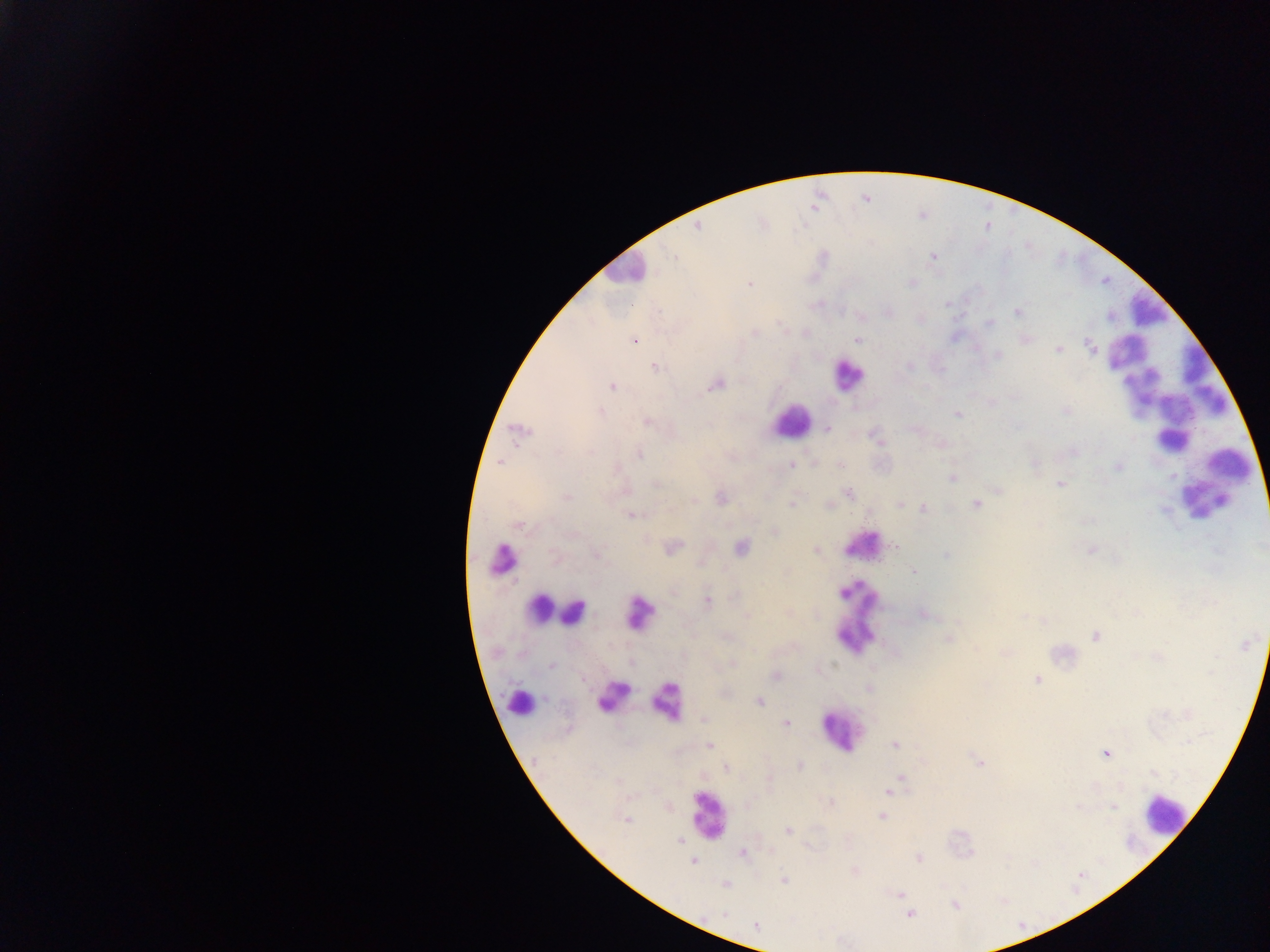

capture = mobile-phone photograph through a microscope
malaria parasite locations = approximate centers as {x, y} in pixels: {866, 199}, {697, 227}, {674, 257}, {932, 258}, {749, 283}, {910, 283}, {946, 304}, {887, 312}, {1017, 313}, {861, 316}, {988, 322}, {634, 340}, {858, 340}, {1025, 340}, {1091, 348}, {1058, 349}, {998, 355}, {909, 365}, {655, 367}, {715, 385}, {612, 386}, {991, 402}, {598, 409}, {1067, 410}, {956, 414}, {647, 422}, {826, 428}, {915, 428}, {518, 431}, {876, 438}, {941, 444}, {1074, 451}, {639, 454}, {500, 461}, {813, 464}, {839, 465}, {1035, 465}, {1118, 465}, {790, 466}, {953, 478}, {656, 484}, {1060, 484}, {997, 489}, {848, 493}, {565, 497}, {721, 498}, {691, 502}, {791, 503}, {827, 504}, {899, 504}, {976, 504}, {923, 508}, {631, 515}, {1084, 520}, {519, 524}, {775, 531}, {895, 546}, {671, 548}, {740, 548}, {1091, 549}, {816, 550}, {946, 554}, {701, 562}, {914, 571}, {706, 601}, {924, 614}, {1022, 615}, {1097, 636}, {948, 640}, {1004, 652}, {733, 663}, {551, 664}, {775, 676}, {1036, 679}, {868, 688}, {758, 701}, {703, 718}, {785, 724}, {894, 744}, {710, 745}, {1105, 754}, {979, 764}, {799, 766}, {726, 767}, {901, 776}, {888, 791}, {1112, 805}, {882, 816}, {627, 820}, {788, 830}, {679, 840}, {742, 853}, {918, 858}, {693, 861}, {853, 870}, {783, 879}, {724, 884}, {899, 894}, {955, 905}, {909, 913}, {725, 916}, {755, 925}
leukocyte locations = approximate centers as {x, y} in pixels: {626, 271}, {1148, 307}, {847, 375}, {1170, 385}, {791, 422}, {1173, 439}, {1228, 464}, {1216, 476}, {1206, 498}, {862, 544}, {501, 559}, {540, 609}, {556, 611}, {573, 611}, {639, 612}, {856, 618}, {612, 695}, {667, 700}, {520, 702}, {840, 731}, {1163, 813}, {707, 815}
country = Ghana
image size = 1270×952 pixels
preparation = thick blood smear
field of view = single